Evaluate for Plasmodium parasites.
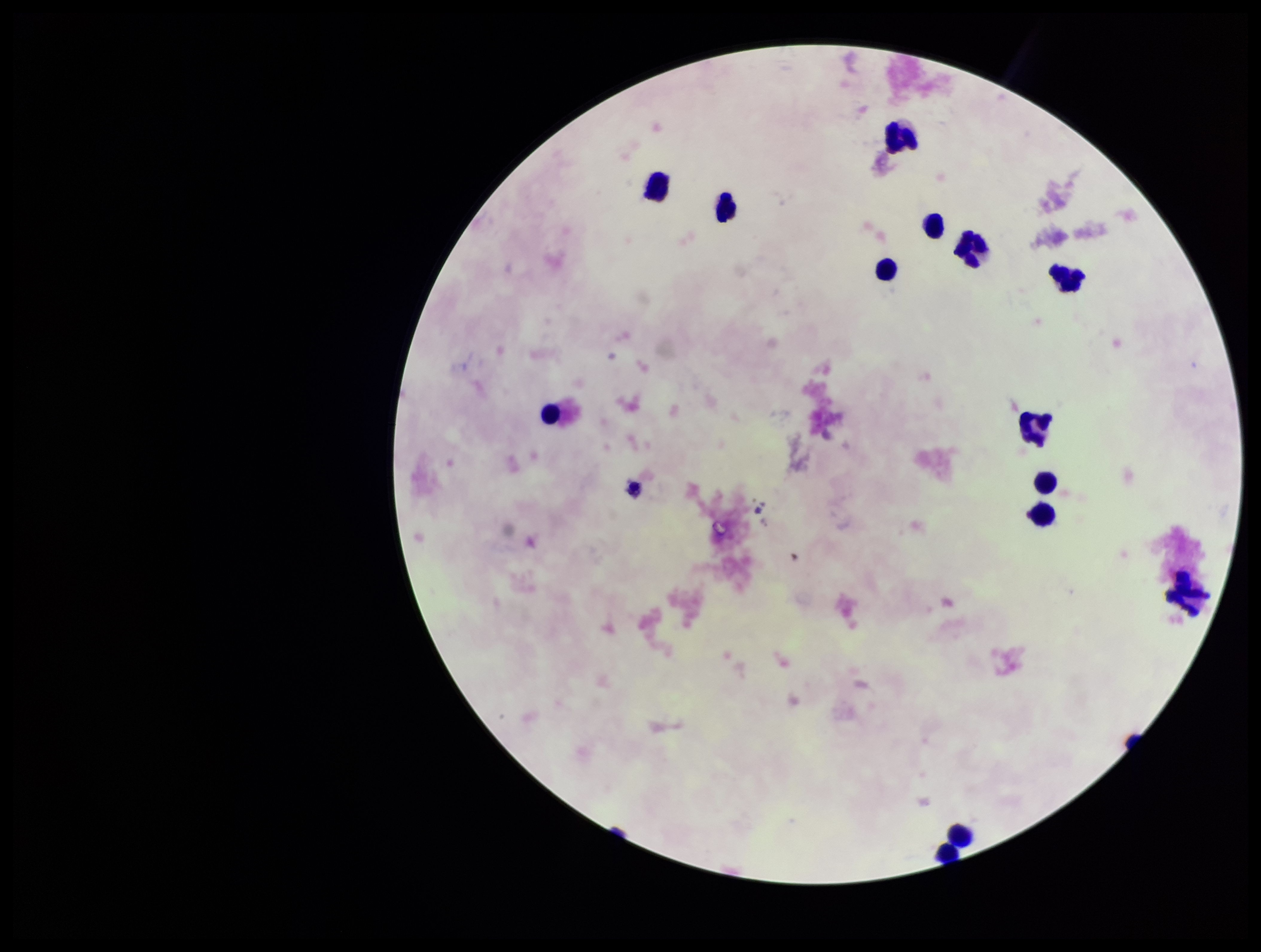
None identified.

Preparation: thick. Smartphone photograph taken through the eyepiece of a microscope. Patient malaria status: negative. Parasite count: 0. Image is 1261×952 pixels. Giemsa stain. Single field of view. Leukocyte count: 14.